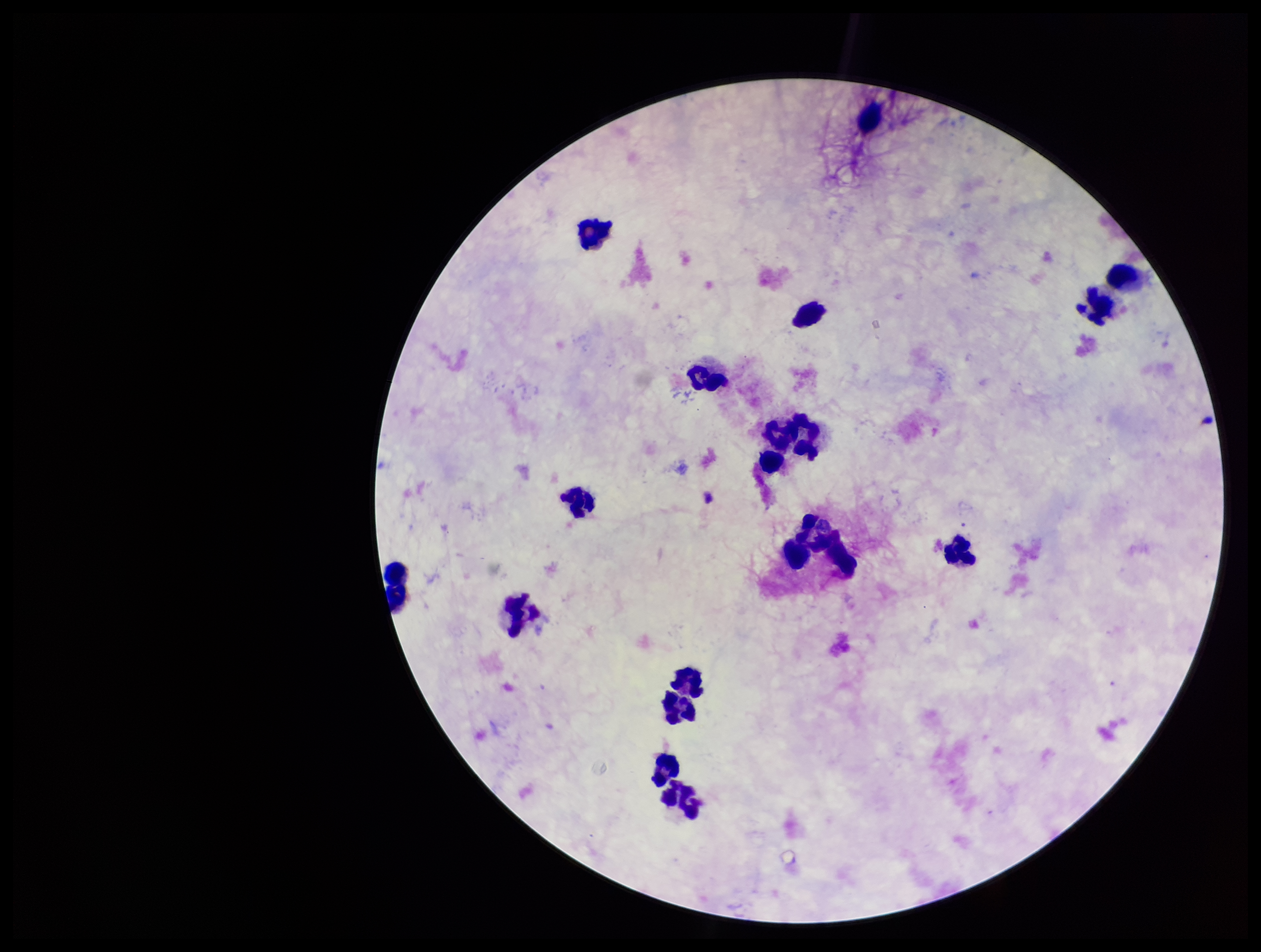

Patient malaria status: negative. Image is 1261×952 pixels. Preparation: thick. Single field of view. Giemsa stain. Plasmodium parasites: none identified. Smartphone photograph taken through the eyepiece of a microscope. Leukocyte count: 18. Parasite count: 0.